Outline platelets.
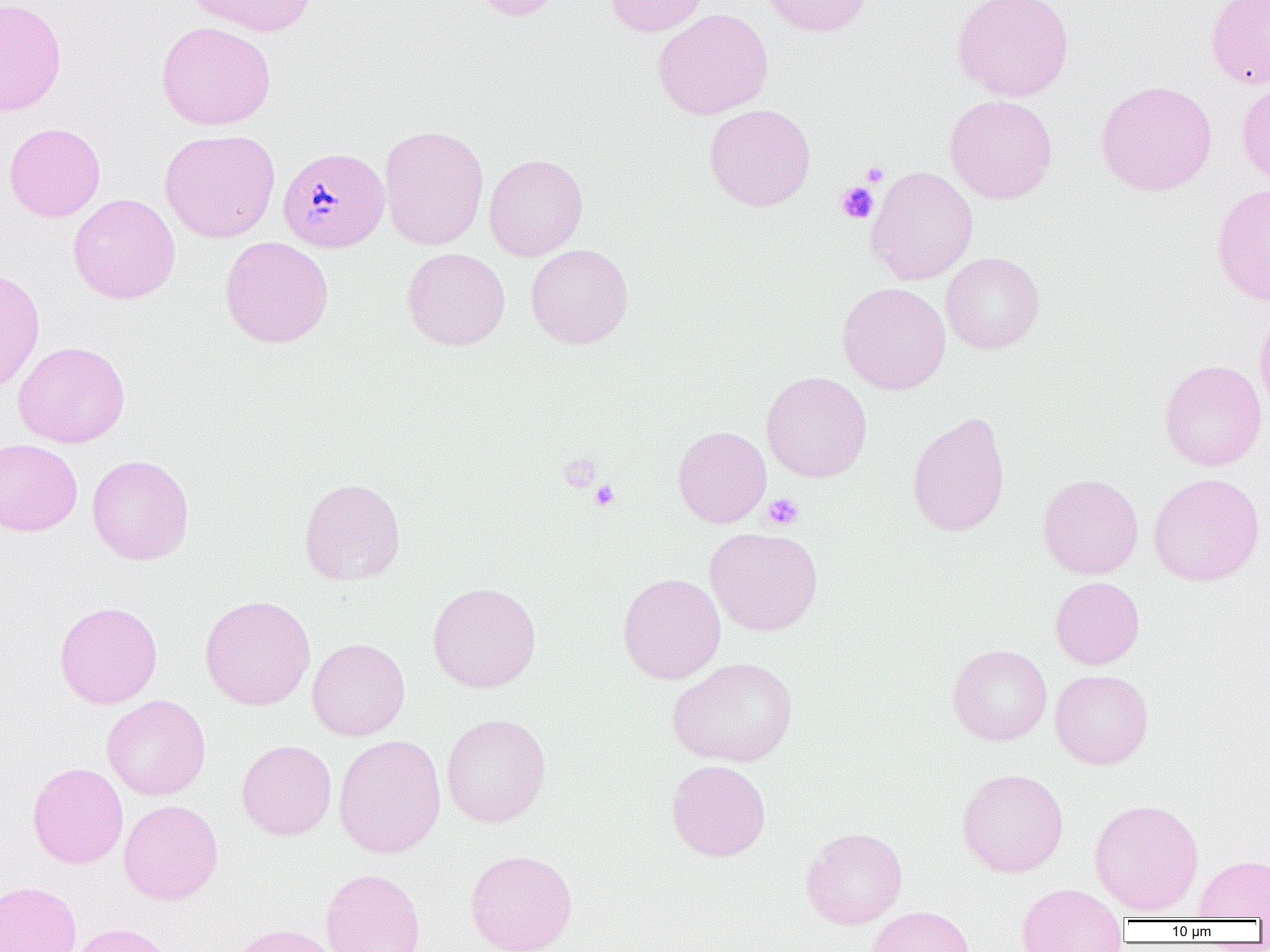
Approximate bounding boxes as [x1, y1, x2, y2] in pixels.
Platelets: [861, 162, 889, 186], [836, 182, 879, 224], [559, 452, 601, 493], [590, 480, 620, 511], [763, 493, 804, 530].

Plasmodium malariae-infected red blood cell locations: [277, 147, 389, 254]. Uninfected red blood cell locations: [0, 0, 67, 116], [185, 0, 315, 37], [470, 0, 565, 21], [604, 0, 710, 37], [758, 0, 872, 37], [953, 0, 1074, 102], [1206, 0, 1270, 90], [653, 8, 774, 119], [156, 21, 276, 130], [1096, 80, 1217, 197], [1236, 81, 1270, 186], [945, 94, 1058, 204], [704, 104, 816, 211], [4, 122, 105, 222], [379, 124, 489, 251], [160, 129, 280, 243], [484, 153, 589, 261], [866, 166, 978, 285], [1211, 182, 1270, 307], [68, 193, 181, 304], [220, 237, 334, 348], [525, 243, 634, 349], [402, 247, 511, 351], [941, 252, 1044, 354], [0, 269, 45, 396], [837, 282, 951, 395], [1254, 302, 1270, 420], [12, 341, 130, 449], [1160, 359, 1267, 471], [761, 371, 872, 483], [907, 410, 1011, 537], [672, 425, 771, 528], [0, 438, 83, 536], [86, 454, 194, 565], [1149, 472, 1265, 586], [1038, 473, 1144, 579], [298, 477, 406, 586], [705, 527, 823, 636], [617, 572, 726, 684], [1050, 577, 1145, 669], [427, 582, 542, 693], [200, 595, 315, 711], [54, 601, 163, 709], [307, 638, 410, 741], [947, 644, 1052, 745], [666, 657, 800, 767], [1050, 669, 1154, 770], [102, 695, 211, 800], [441, 713, 551, 829], [334, 734, 446, 858], [237, 739, 337, 841], [666, 760, 771, 862], [27, 762, 128, 869], [957, 768, 1069, 877], [1089, 799, 1204, 916], [119, 800, 223, 905], [800, 826, 908, 929], [465, 849, 578, 952], [1194, 855, 1270, 920], [320, 868, 427, 952], [0, 880, 82, 952], [1016, 883, 1128, 952], [866, 905, 975, 952], [68, 922, 174, 952], [226, 923, 342, 952]. Slide-level diagnosis: Plasmodium malariae. Image is 1270×952 pixels. Optical microscopy. Captured at 1000x magnification. One field of a larger specimen. Thin blood film.